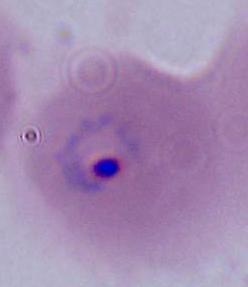
identification = Plasmodium
modality = photomicrograph
magnification = 400x or 1000x